Point out each Plasmodium parasite.
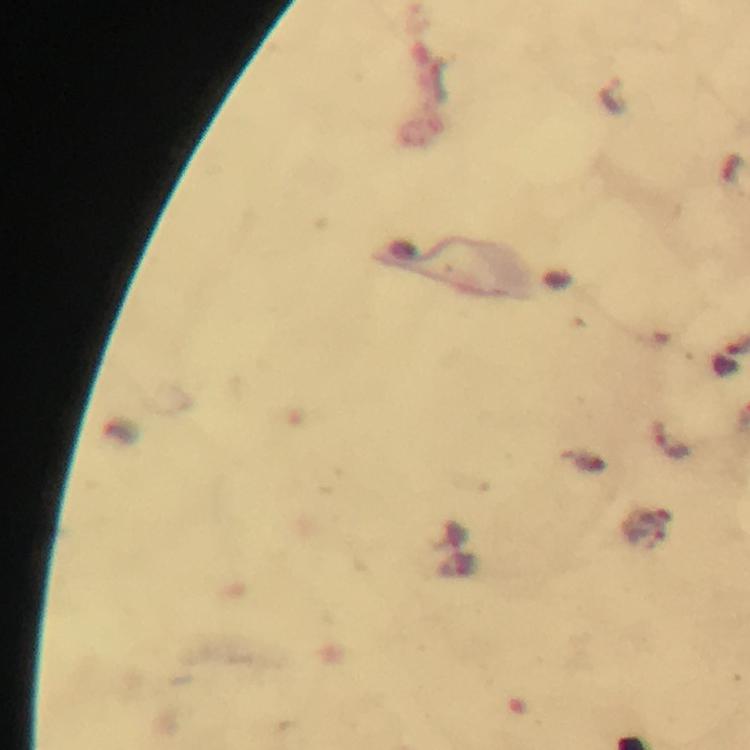
Approximate object centers, in pixels from the top-left corner.
Plasmodium parasites: (x=727, y=359), (x=670, y=439).

Immersion oil was used. Thick smear. From a diagnostic examination for malaria. Image is 750×750 pixels. Giemsa stain. A crop from one field of view. At 100x magnification. Photographed with a smartphone mounted on the microscope.